Classify this cell by malaria status.
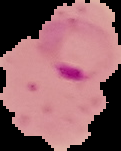
It is parasitized.

Summary:
  - Image size: 121×151 pixels
  - Preparation: thin blood smear
  - Image type: segmented cell region on a black background